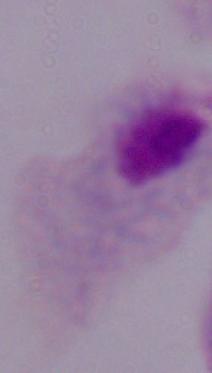 A trichomonad is shown. Micrograph. Captured at 1000x magnification.